Locate every blood parasite and identify its species.
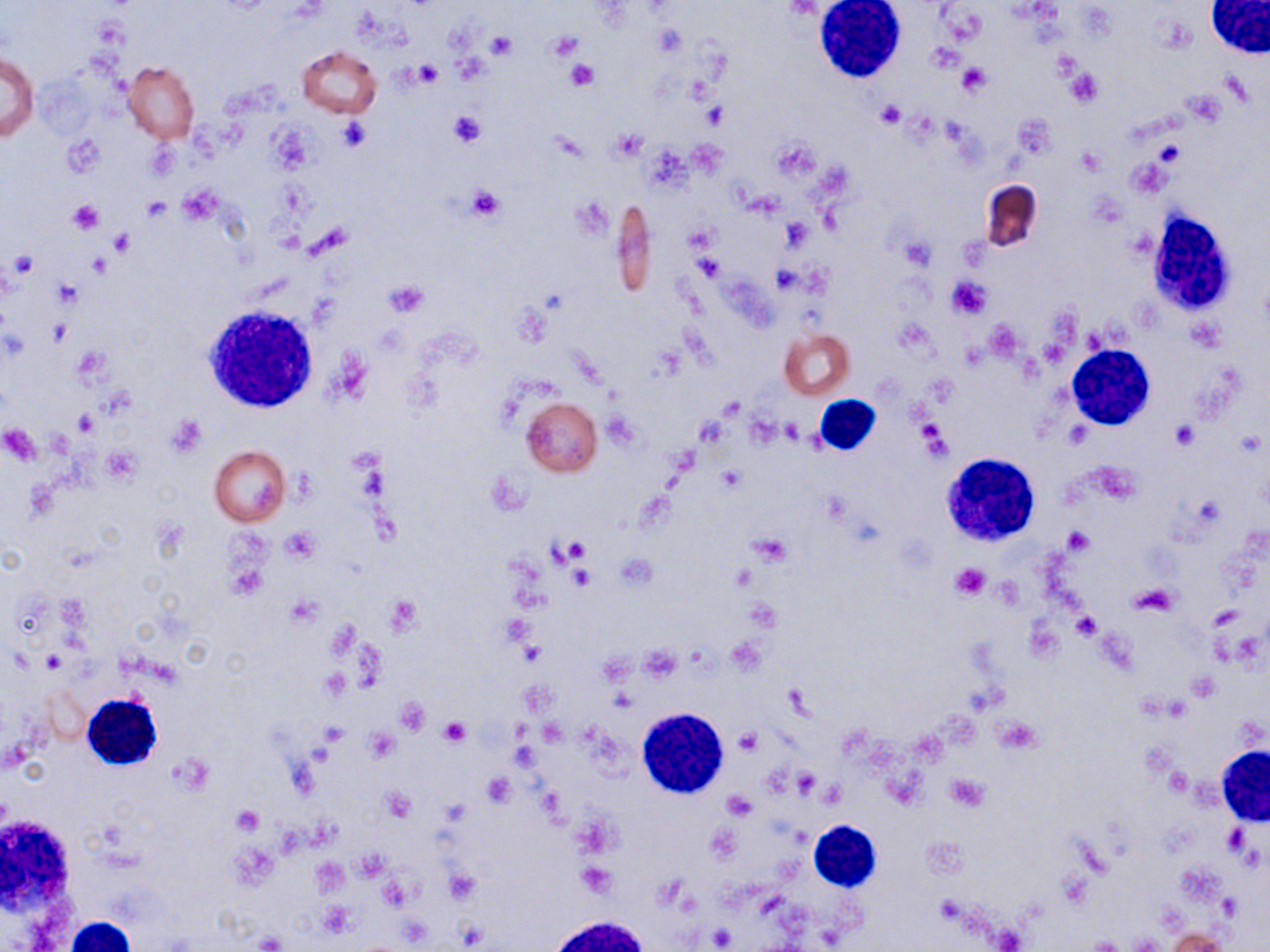

No blood parasites observed.

Approximate bounding boxes as (x1,y1)-(x2,y2) corner pairs in pixels. Platelet locations: (652,23)-(687,58), (547,30)-(583,62), (488,31)-(517,59), (565,59)-(599,92), (412,61)-(443,87), (958,65)-(990,95), (1066,70)-(1103,107), (876,100)-(905,128), (701,103)-(728,128), (449,111)-(484,146), (336,118)-(371,152), (62,133)-(105,176), (466,185)-(506,221), (176,187)-(222,222), (142,196)-(172,221), (574,196)-(613,238), (67,200)-(103,234), (781,219)-(812,252), (687,226)-(716,255), (109,230)-(135,255), (900,235)-(935,269), (7,253)-(36,280), (695,254)-(724,282), (946,275)-(992,320), (54,278)-(83,307), (382,278)-(429,318), (167,415)-(206,456), (917,419)-(951,460), (1172,422)-(1199,447), (0,423)-(41,464), (718,465)-(747,492), (280,526)-(320,564), (1061,528)-(1094,555), (750,533)-(793,568), (561,538)-(591,565), (225,562)-(268,601), (568,562)-(597,590), (729,563)-(756,591), (949,563)-(991,601), (1072,613)-(1101,639), (40,651)-(65,674), (322,668)-(351,699), (1187,670)-(1219,700), (395,698)-(432,735), (439,717)-(472,747), (320,721)-(350,746), (735,727)-(762,755), (364,729)-(399,762), (790,768)-(821,797), (482,771)-(515,806), (945,773)-(989,812), (382,786)-(416,823), (724,790)-(757,819), (232,806)-(264,835), (1223,826)-(1247,854), (576,861)-(619,897), (319,900)-(355,937), (257,933)-(285,951). Uninfected red blood cell locations: (297,45)-(382,118), (1,52)-(39,144), (124,61)-(200,144), (979,180)-(1042,253), (611,198)-(658,299), (779,329)-(855,401), (521,397)-(603,477), (209,445)-(290,526), (1167,929)-(1227,951). White blood cell locations: (814,0)-(908,84), (1204,0)-(1269,58), (1145,206)-(1240,322), (205,305)-(320,413), (1067,344)-(1155,429), (813,396)-(880,456), (941,453)-(1041,547), (81,694)-(162,769), (637,708)-(729,798), (1216,746)-(1270,827), (0,818)-(77,917), (809,819)-(881,890), (64,917)-(138,952). Slide-level diagnosis: negative for blood parasites. Optical microscopy. Image is 1270×952 pixels. 1000x magnification. May-Grünwald-Giemsa-stained preparation. Thin blood smear. One field of a larger specimen.